Look for Plasmodium parasites.
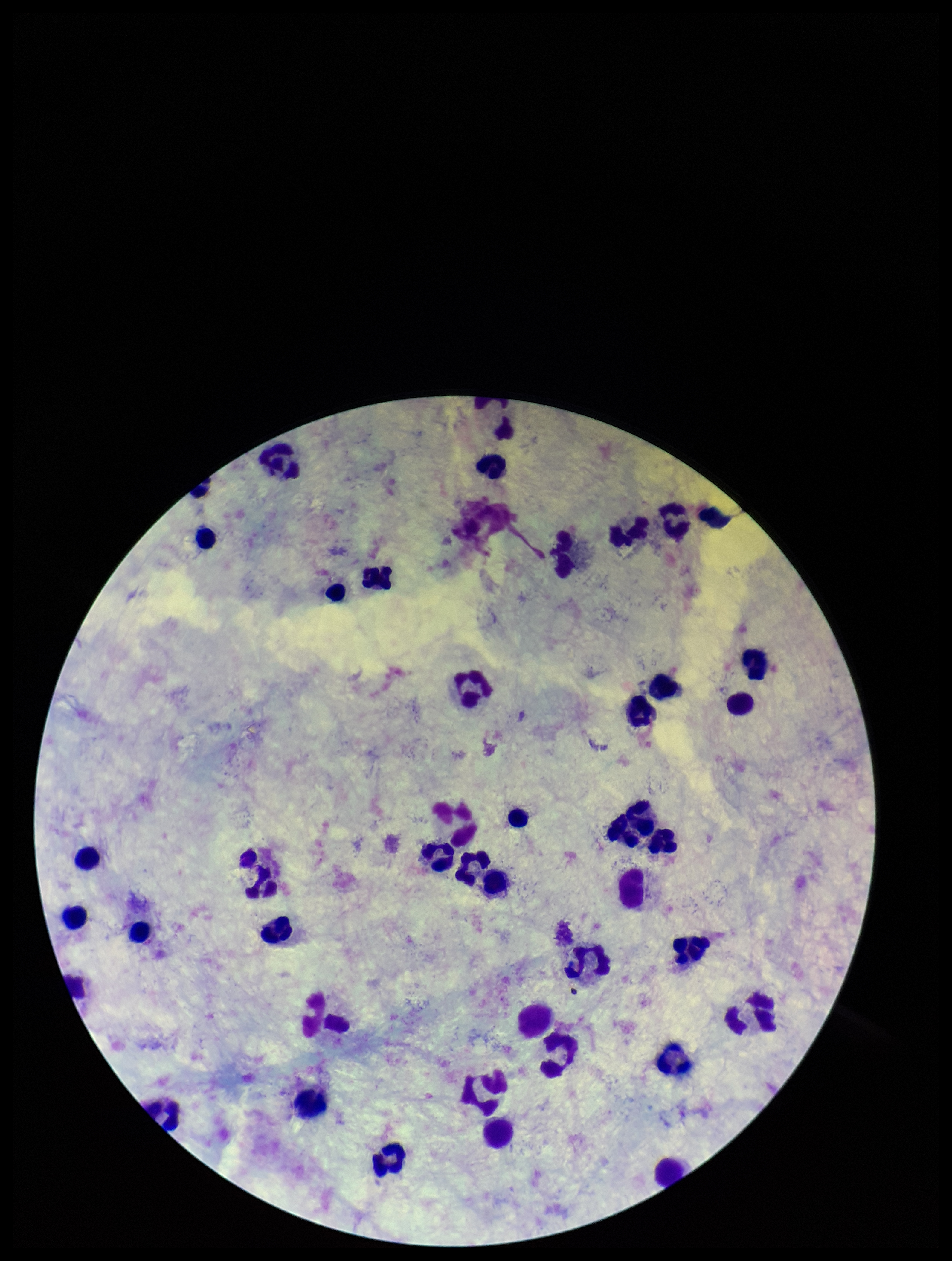
None detected.

Parasite count: 0. Image is 952×1261 pixels. Smartphone photograph taken through the eyepiece of a microscope. One field from this slide. Preparation: thick blood smear. Patient malaria status: negative. Giemsa stain. Leukocyte count: 41.